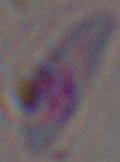 Toxoplasma gondii is shown. Micrograph. Captured at 1000x magnification.